State which parasite is depicted.
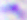

This is Toxoplasma gondii.

Photomicrograph. Captured at 400x magnification.